Classify this cell by malaria status.
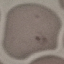
It is uninfected.

Giemsa-stained preparation. Photographed with a smartphone camera at the microscope eyepiece. Cell patch, automatically extracted from a larger field of view and resized to 64 × 64 pixels. Thin smear of blood.